Classify this cell by malaria status.
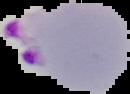

Parasitized.

Summary:
  - Preparation: thin blood film
  - Image type: segmented cell region on a black background
  - Image size: 130×94 pixels